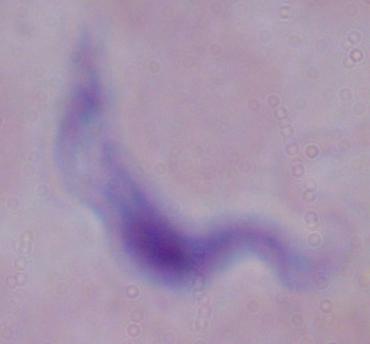
Photomicrograph. A trypanosome is seen. 1000x magnification.